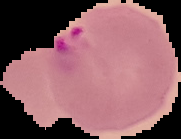 From a thin blood film. Malaria status: parasitized. Image is 181×139 pixels. Cell region segmented out of the field of view; the surrounding area is masked to black.